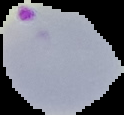
Image is 124×115 pixels. Cell region segmented out of the field of view; the surrounding area is masked to black. Malaria status: parasitized. From a thin blood film.